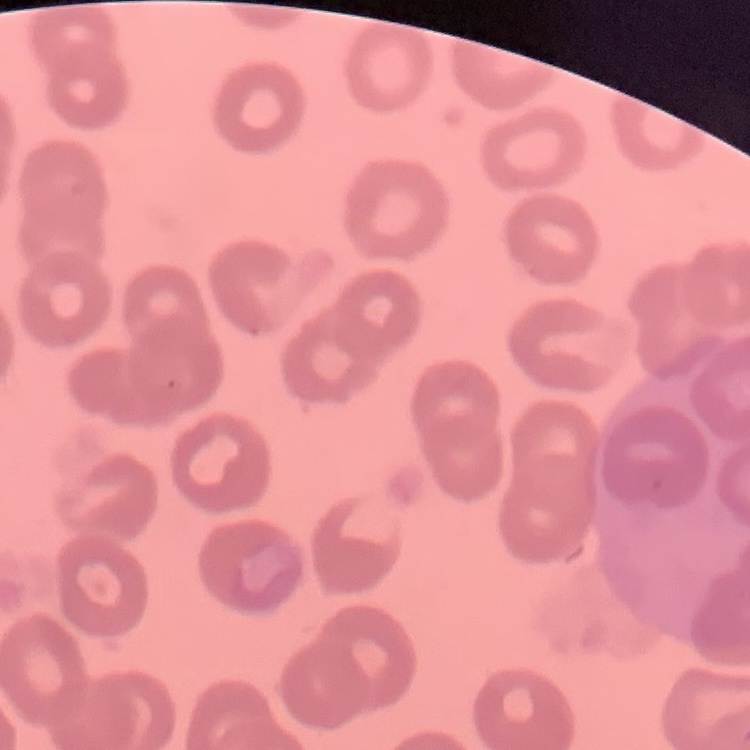

Summary:
  - Erythrocyte morphology: no rouleaux formation
  - Preparation: thin peripheral smear
  - Image type: one tile cut from a larger photomicrograph
  - Stain: Field's or Giemsa